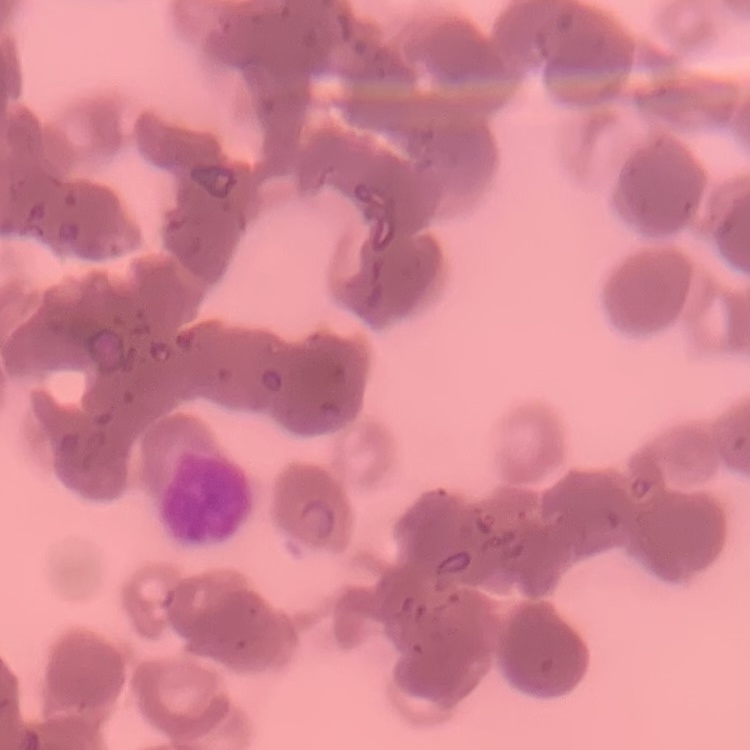

Summary:
  - Red blood cell morphology: rouleaux formation
  - Preparation: thin blood smear
  - Stain: Field's or Giemsa
  - Image type: square crop of a larger photomicrograph